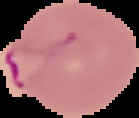

preparation = thin blood smear
image size = 139×118 pixels
result = Plasmodium parasites detected
image type = segmented cell region on a black background